Outline each blood parasite and name the species.
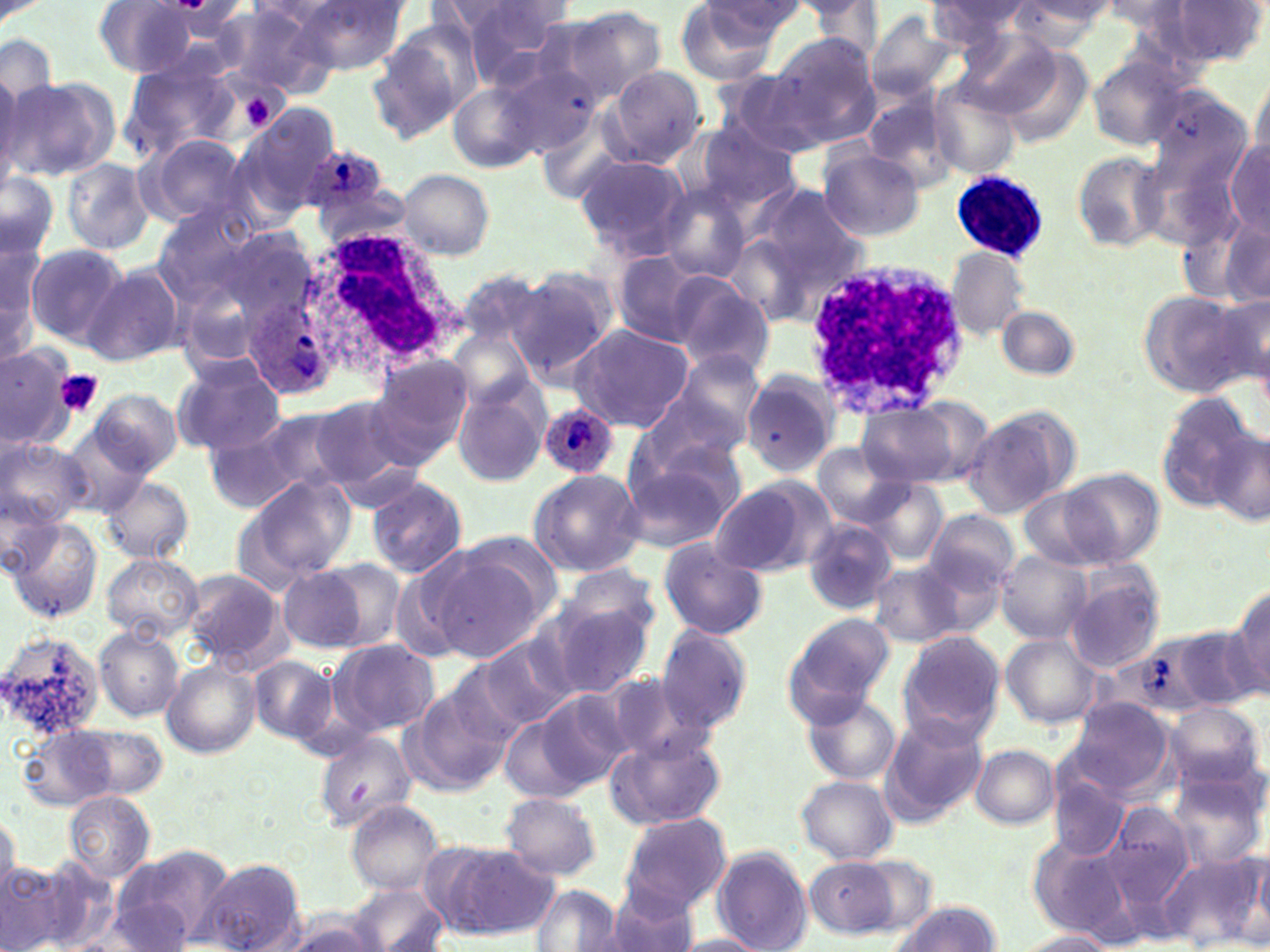
Approximate bounding boxes as (x1,y1)-(x2,y2) corner pairs in pixels.
Plasmodium ovale-infected red blood cells: (299,144)-(384,216), (244,299)-(334,400), (538,401)-(619,481).
No Plasmodium falciparum, Plasmodium malariae, Plasmodium vivax, Babesia divergens, or Trypanosoma brucei observed.

Summary:
  - Platelet locations: (242,96)-(274,127), (52,369)-(103,418)
  - Uninfected red blood cell locations: (291,0)-(408,74), (699,0)-(807,50), (803,0)-(886,61), (926,0)-(1034,46), (1099,0)-(1191,38), (1166,0)-(1267,66), (93,1)-(196,78), (1008,1)-(1115,47), (462,2)-(569,80), (217,4)-(338,96), (672,4)-(783,84), (558,6)-(668,102), (865,11)-(958,99), (955,27)-(1063,118), (370,29)-(476,142), (765,32)-(881,144), (0,33)-(58,119), (996,49)-(1094,151), (1086,55)-(1190,151), (120,58)-(243,165), (475,64)-(597,165), (602,65)-(705,169), (1247,69)-(1269,172), (223,70)-(290,135), (719,70)-(832,159), (0,71)-(33,188), (1,75)-(117,182), (450,82)-(541,174), (929,83)-(1022,181), (859,92)-(962,194), (234,104)-(341,213), (690,123)-(802,213), (139,133)-(253,228), (1226,141)-(1270,236), (818,149)-(925,242), (1072,150)-(1167,251), (575,155)-(696,262), (61,157)-(155,256), (398,168)-(494,261), (0,172)-(59,259), (659,184)-(751,281), (750,185)-(866,291), (152,203)-(261,302), (1217,219)-(1270,307), (721,228)-(829,327), (24,243)-(131,349), (0,247)-(43,364), (945,247)-(1030,339), (610,250)-(709,348), (81,263)-(186,367), (511,270)-(618,381), (461,272)-(545,356), (667,274)-(773,377), (1138,290)-(1251,398), (1210,290)-(1270,394), (996,305)-(1079,381), (566,324)-(694,431), (451,334)-(540,428), (0,343)-(77,450), (664,350)-(766,450), (170,354)-(287,455), (370,355)-(475,461), (740,371)-(841,477), (454,383)-(548,488), (633,383)-(753,477), (88,388)-(181,477), (1154,395)-(1256,509), (310,396)-(412,492), (857,405)-(961,486), (241,406)-(356,502), (964,411)-(1075,519), (60,423)-(153,513), (208,423)-(312,514), (1209,432)-(1268,527), (0,436)-(90,530), (812,442)-(910,528), (620,444)-(745,551), (1061,468)-(1165,566), (527,469)-(644,578), (101,475)-(193,563), (247,475)-(354,581), (708,477)-(833,579), (367,478)-(467,577), (860,478)-(948,565), (1017,489)-(1111,565), (1,490)-(61,575), (923,510)-(1019,599), (7,517)-(103,623), (802,520)-(896,614), (657,540)-(768,640), (995,550)-(1091,644), (432,554)-(546,664), (101,555)-(200,641), (388,557)-(479,665), (321,560)-(408,649), (559,564)-(661,645), (869,565)-(963,647), (279,566)-(370,651), (183,569)-(286,669), (1064,569)-(1164,673), (1226,585)-(1270,693), (546,599)-(653,699), (782,614)-(892,722), (658,626)-(753,732), (1171,626)-(1260,712), (95,627)-(183,722), (0,629)-(109,739), (897,630)-(1007,745), (477,635)-(575,732), (1001,635)-(1101,728), (331,638)-(439,737), (249,656)-(339,744), (163,660)-(261,757), (600,671)-(712,766), (410,685)-(509,791), (534,688)-(632,789), (803,694)-(901,786), (1065,698)-(1178,801), (1165,701)-(1266,791), (503,713)-(594,803), (880,715)-(990,825), (18,724)-(134,811), (315,729)-(419,831), (605,732)-(726,829), (970,744)-(1059,829), (1051,770)-(1127,861), (1167,771)-(1265,871), (796,776)-(897,864), (64,790)-(154,883), (500,791)-(601,882), (345,800)-(445,896), (1104,801)-(1198,909), (0,809)-(20,897), (618,813)-(733,917), (1027,833)-(1140,945), (437,843)-(557,939), (711,846)-(813,951), (107,847)-(231,949), (1158,850)-(1268,948), (1253,853)-(1270,939), (2,857)-(63,952), (200,857)-(308,952), (805,857)-(901,938), (605,884)-(704,952), (347,885)-(450,952), (532,885)-(623,952), (892,900)-(1001,952), (279,911)-(387,952), (1018,931)-(1118,951), (669,933)-(770,951)
  - White blood cell locations: (955,172)-(1044,257), (290,223)-(459,377), (801,258)-(968,416)
  - Slide-level diagnosis: Plasmodium ovale
  - Image size: 1270×952 pixels
  - Stain: May-Grünwald-Giemsa
  - Magnification: 1000x
  - Preparation: thin blood film
  - Field of view: single
  - Modality: optical microscopy